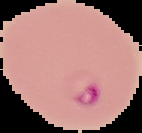

result: Plasmodium parasites detected
image_type: cell region segmented out of the field of view; surrounding area masked to black
image_size: 142×133 pixels
preparation: thin blood smear